Report the malaria status of this cell.
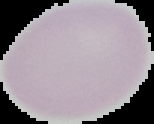

Uninfected.

{
  "image_type": "segmented cell region on a black background",
  "image_size": "154×124 pixels",
  "preparation": "thin blood film"
}